Identify the parasite.
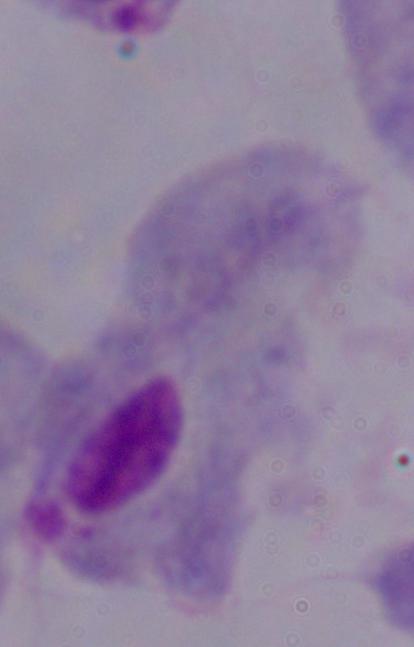
This is a trichomonad.

modality = micrograph
magnification = 1000x